Comment on the morphology of the erythrocytes.
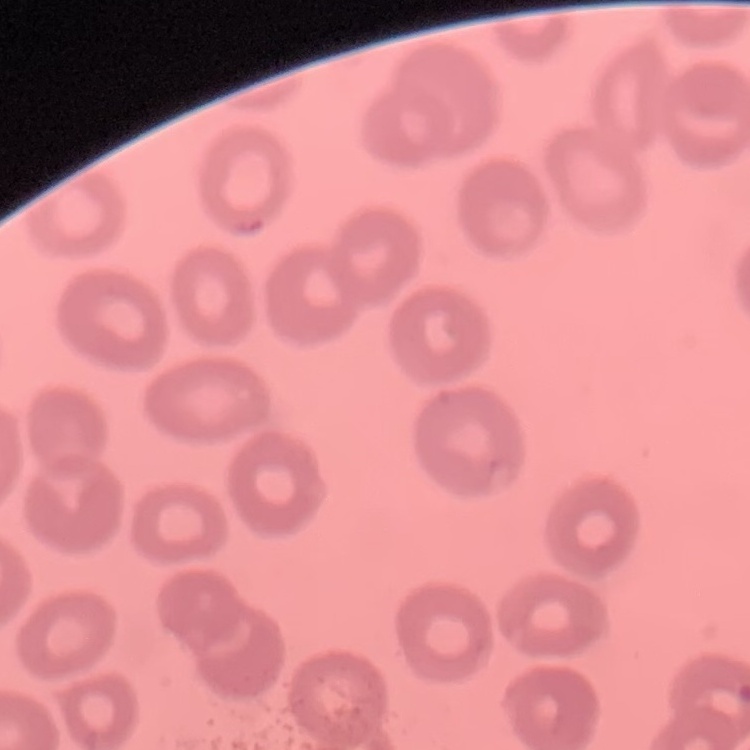
They show no rouleaux formation.

image type = square crop of a larger photomicrograph
stain = Field's or Giemsa
preparation = thin peripheral smear